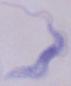

modality: photomicrograph
magnification: 1000x
identification: trypanosome